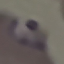
Summary:
  - Malaria status: parasitized
  - Preparation: thin smear
  - Image type: cell patch, automatically extracted from a larger field of view and resized to 64 × 64 pixels
  - Stain: Giemsa
  - Capture: smartphone through the microscope eyepiece